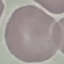 Result: negative for malaria parasites. Giemsa-stained preparation. Thin smear of blood. Cell patch, automatically extracted from a larger field of view and resized to 64 × 64 pixels. Photographed with a smartphone camera at the microscope eyepiece.